State which parasite is depicted.
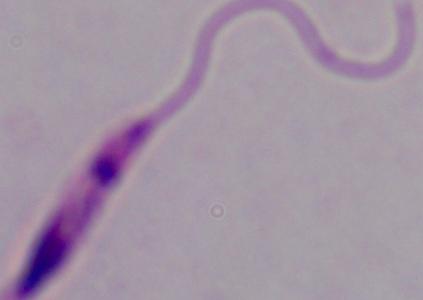

This is Leishmania.

1000x magnification. Photomicrograph.